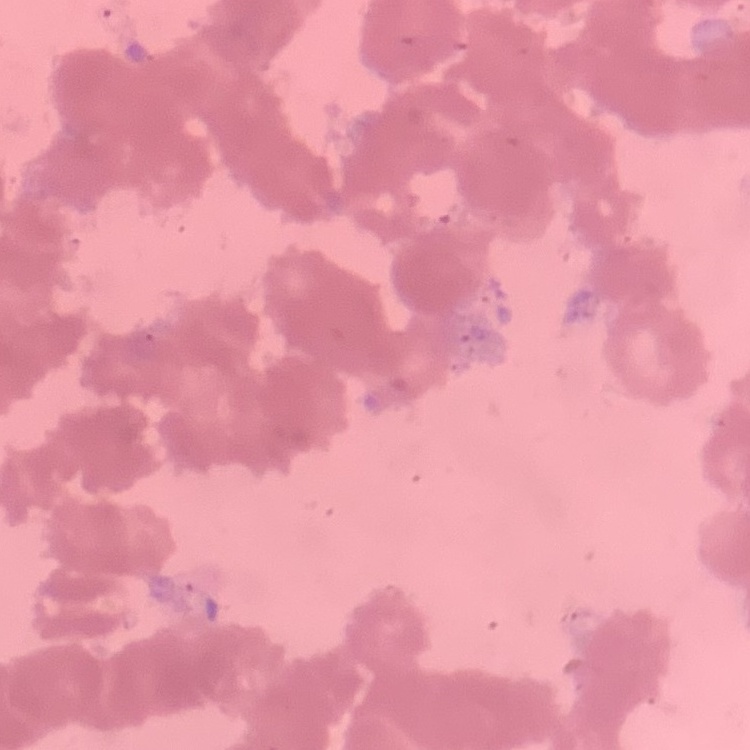
red blood cell morphology = rouleaux formation
image type = one tile cut from a larger photomicrograph
preparation = thin peripheral smear
stain = Field's or Giemsa